Give the preparation type.
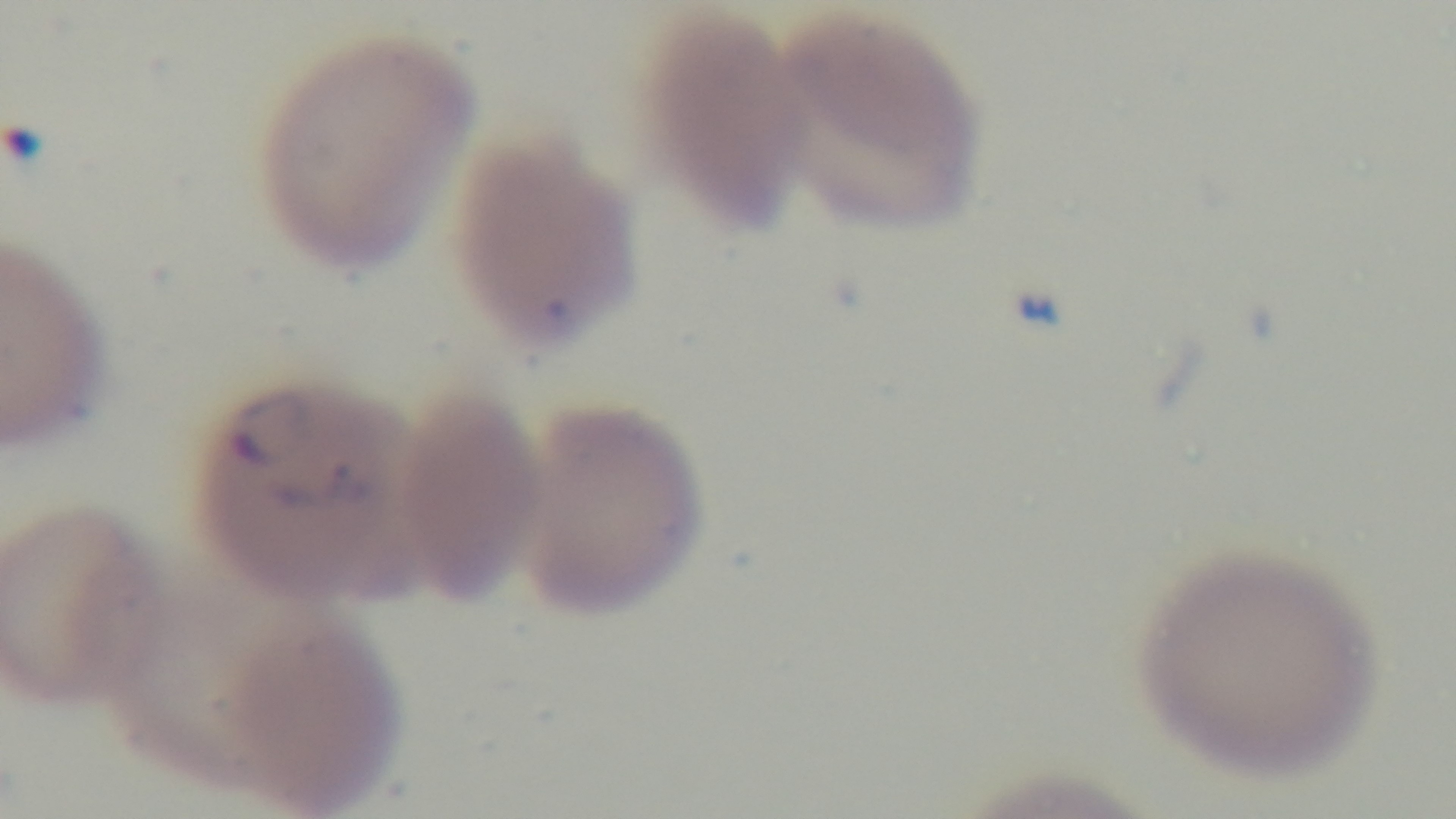
Thin.

Summary:
  - Modality: light microscopy
  - Field of view: one from the slide
  - Objective: 100x oil immersion
  - Malaria status: positive
  - Stain: Giemsa
  - Capture: mounted 4K digital camera